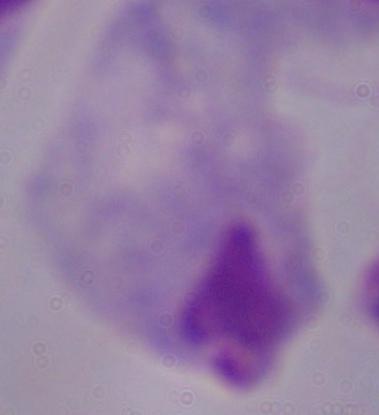

Summary:
  - Modality: photomicrograph
  - Magnification: 1000x
  - Identification: trichomonad